Identify the parasite.
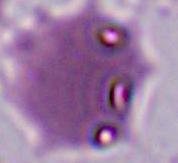
This is Plasmodium.

Summary:
  - Magnification: 400x or 1000x
  - Modality: photomicrograph